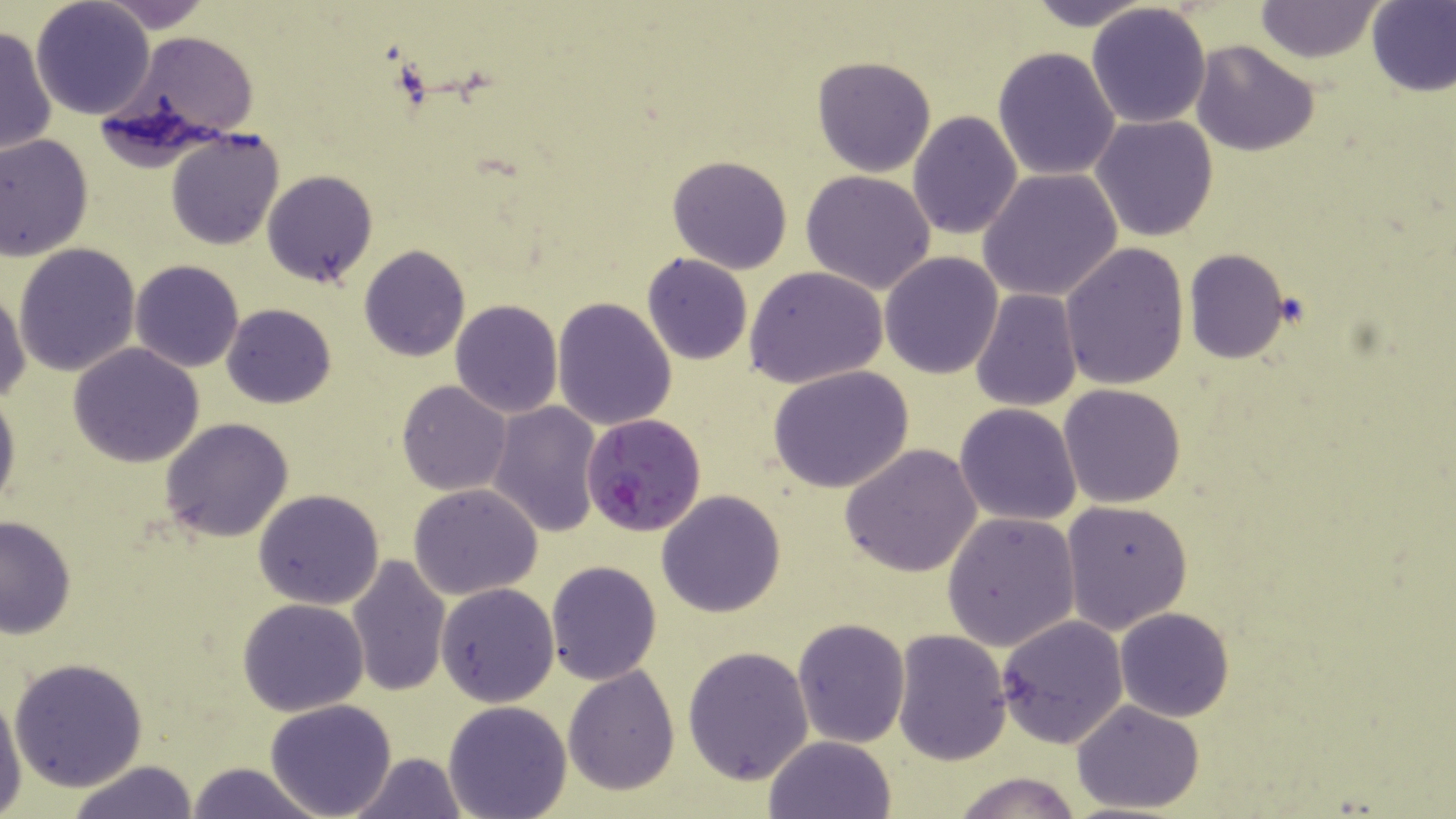
Summary:
  - Coordinate format: approximate bounding boxes as [x1, y1, x2, y2] in pixels
  - Plasmodium falciparum-infected red blood cell locations: [579, 413, 707, 536]
  - Uninfected red blood cell locations: [97, 0, 214, 30], [1024, 0, 1157, 31], [31, 1, 156, 121], [1252, 2, 1386, 64], [1366, 2, 1456, 95], [1085, 3, 1212, 130], [1, 25, 56, 158], [115, 31, 262, 145], [1192, 39, 1320, 157], [992, 45, 1122, 182], [811, 55, 936, 177], [906, 110, 1023, 240], [1091, 115, 1219, 241], [166, 128, 288, 249], [0, 133, 94, 260], [666, 154, 792, 275], [978, 168, 1123, 304], [262, 170, 378, 289], [800, 170, 937, 295], [1059, 242, 1190, 390], [14, 243, 141, 376], [358, 245, 471, 363], [1184, 248, 1291, 364], [880, 252, 1004, 377], [642, 253, 752, 365], [131, 260, 243, 372], [746, 266, 888, 390], [93, 283, 226, 428], [0, 287, 29, 404], [970, 290, 1082, 410], [552, 297, 676, 431], [450, 300, 563, 419], [222, 303, 336, 408], [68, 343, 205, 468], [770, 366, 914, 494], [396, 381, 512, 495], [0, 382, 20, 516], [1058, 383, 1187, 508], [488, 401, 602, 538], [954, 403, 1082, 526], [159, 416, 296, 542], [840, 445, 983, 578], [409, 482, 543, 599], [252, 489, 385, 609], [656, 489, 786, 618], [1060, 499, 1192, 635], [942, 511, 1081, 650], [0, 515, 76, 638], [346, 554, 451, 697], [546, 560, 663, 684], [435, 583, 558, 707], [238, 598, 368, 715], [1114, 607, 1234, 721], [996, 614, 1128, 748], [791, 617, 909, 747], [893, 628, 1012, 764], [683, 644, 814, 784], [8, 658, 149, 791], [563, 666, 680, 794], [0, 690, 24, 814], [264, 698, 397, 819], [442, 699, 572, 819], [1071, 701, 1206, 816], [762, 736, 898, 819], [347, 752, 468, 819], [64, 760, 198, 819], [184, 762, 327, 817], [950, 770, 1084, 819]
  - Slide-level diagnosis: Plasmodium falciparum
  - Image size: 1456×819 pixels
  - Field of view: single
  - Magnification: 1000x
  - Modality: optical microscopy
  - Preparation: thin blood smear
  - Stain: May-Grünwald-Giemsa